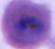

Summary:
  - Modality: micrograph
  - Magnification: 400x or 1000x
  - Identification: Plasmodium